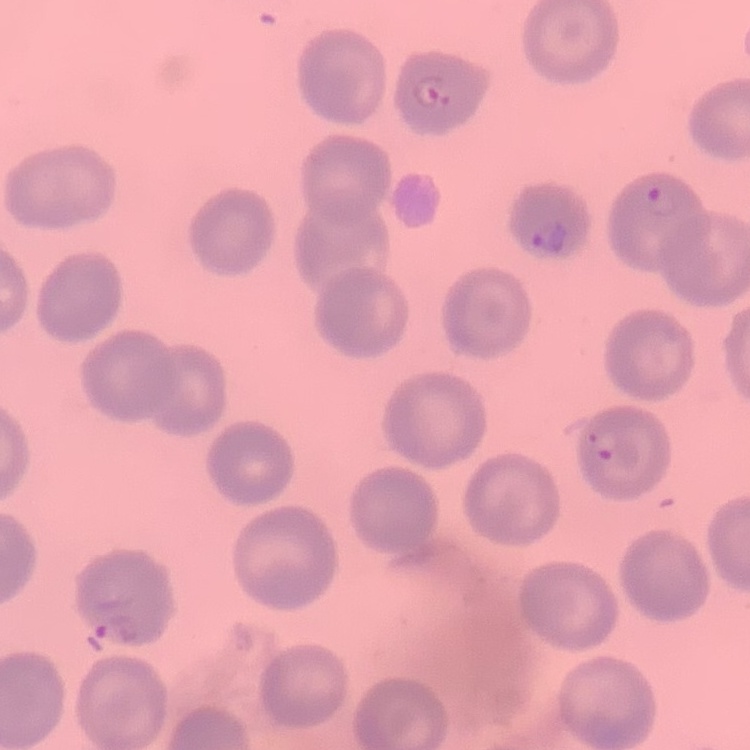
The red blood cells exhibit no rouleaux formation. Stained with either Field's or Giemsa. One tile cut from a larger photomicrograph. Thin blood smear.